Outline each uninfected red blood cell.
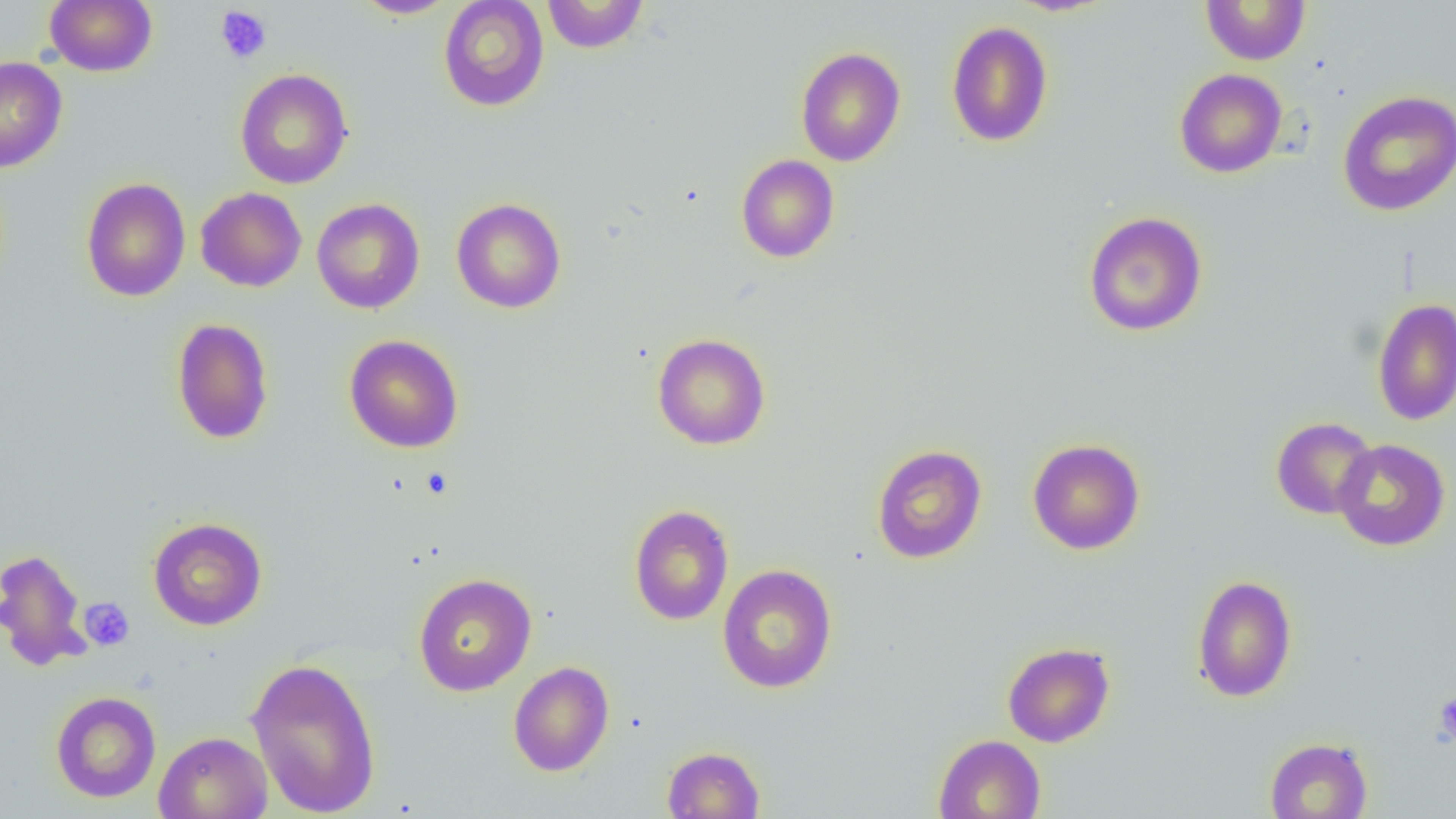
Approximate bounding boxes as named x1/y1/x2/y2 corners in pixels.
Uninfected red blood cells: (x1=44, y1=0, x2=157, y2=76), (x1=351, y1=0, x2=459, y2=19), (x1=438, y1=0, x2=549, y2=112), (x1=541, y1=0, x2=649, y2=54), (x1=1200, y1=0, x2=1310, y2=65), (x1=946, y1=20, x2=1054, y2=147), (x1=795, y1=47, x2=905, y2=167), (x1=0, y1=56, x2=68, y2=172), (x1=235, y1=68, x2=353, y2=189), (x1=1174, y1=68, x2=1287, y2=178), (x1=1338, y1=89, x2=1456, y2=216), (x1=736, y1=154, x2=840, y2=263), (x1=81, y1=177, x2=191, y2=301), (x1=195, y1=187, x2=307, y2=292), (x1=451, y1=197, x2=567, y2=314), (x1=311, y1=198, x2=425, y2=314), (x1=1083, y1=211, x2=1209, y2=337), (x1=1372, y1=297, x2=1456, y2=426), (x1=171, y1=318, x2=274, y2=444), (x1=651, y1=333, x2=771, y2=450), (x1=343, y1=335, x2=464, y2=453), (x1=1271, y1=417, x2=1378, y2=520), (x1=1028, y1=438, x2=1146, y2=555), (x1=1333, y1=439, x2=1451, y2=552), (x1=871, y1=444, x2=987, y2=564), (x1=629, y1=505, x2=734, y2=626), (x1=148, y1=517, x2=267, y2=630), (x1=0, y1=548, x2=92, y2=672), (x1=717, y1=564, x2=837, y2=694), (x1=413, y1=572, x2=537, y2=696), (x1=1191, y1=575, x2=1298, y2=702), (x1=1002, y1=641, x2=1115, y2=748), (x1=245, y1=655, x2=382, y2=817), (x1=509, y1=661, x2=614, y2=776), (x1=50, y1=691, x2=161, y2=802), (x1=153, y1=731, x2=273, y2=819), (x1=933, y1=734, x2=1047, y2=819), (x1=1264, y1=737, x2=1373, y2=819), (x1=662, y1=745, x2=766, y2=818).

Platelet locations: (x1=214, y1=5, x2=272, y2=64), (x1=79, y1=598, x2=135, y2=651), (x1=1433, y1=691, x2=1456, y2=747). Slide-level diagnosis: negative for blood parasites. 1000x magnification. One field of a larger specimen. Light microscopy. Thin blood smear. Image is 1456×819 pixels.